Give the extent of all Plasmodium falciparum-infected red blood cells.
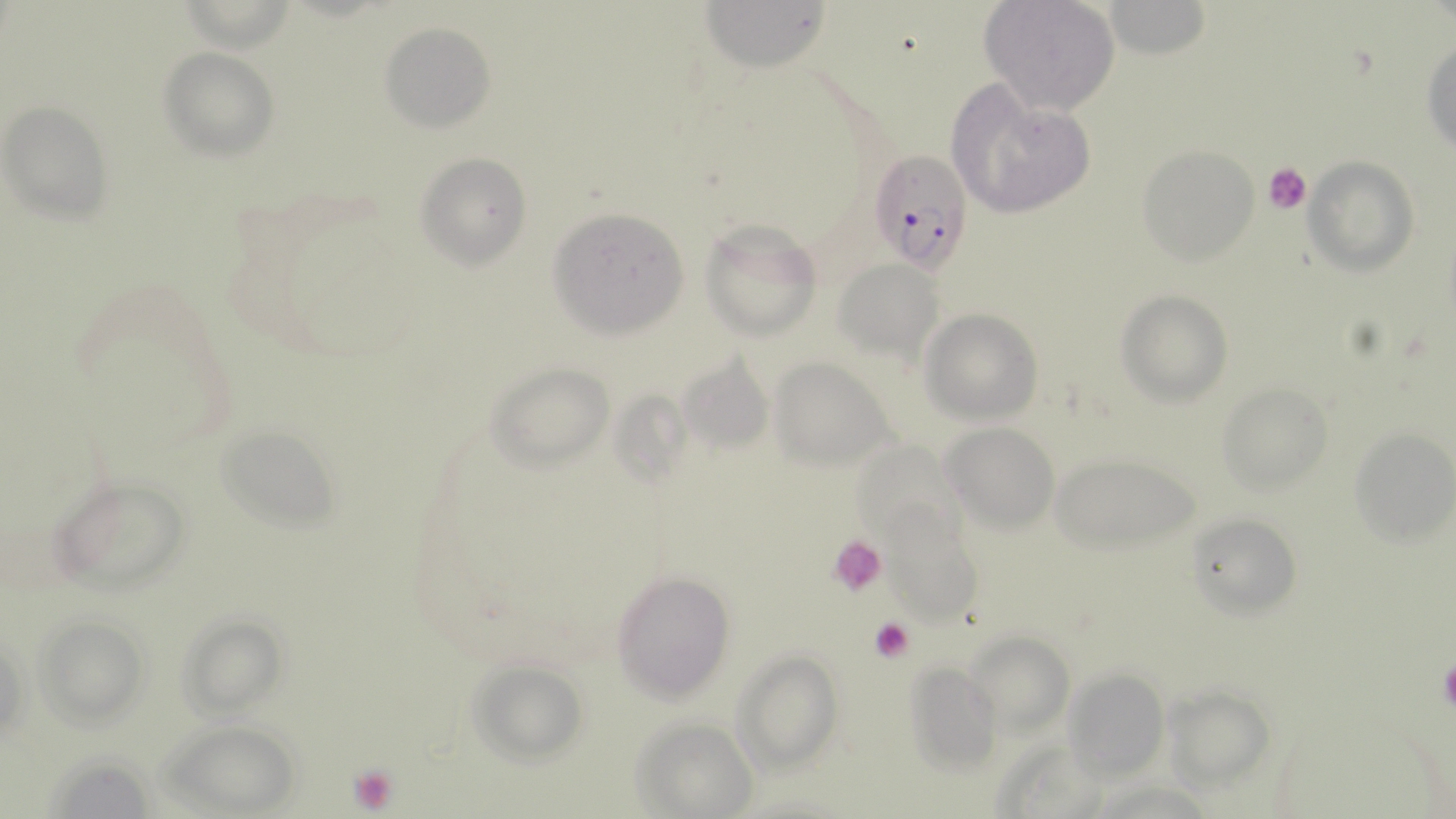

Approximate bounding boxes as (x1,y1)-(x2,y2) corner pairs in pixels.
Plasmodium falciparum-infected red blood cells: (869,148)-(974,273).

slide-level diagnosis = Plasmodium falciparum
magnification = 1000x
uninfected red blood cell locations = approximate bounding boxes as (x1,y1)-(x2,y2) corner pairs in pixels: (700,0)-(832,70), (979,0)-(1120,115), (1099,0)-(1211,60), (380,22)-(496,132), (1422,35)-(1455,157), (159,47)-(279,160), (946,83)-(1099,220), (2,102)-(113,223), (1137,144)-(1259,264), (416,151)-(532,269), (1306,157)-(1418,273), (548,206)-(689,337), (699,219)-(822,340), (835,258)-(946,358), (1118,290)-(1232,405), (920,308)-(1042,425), (677,349)-(774,460), (769,357)-(894,470), (487,361)-(615,469), (1218,382)-(1333,495), (942,423)-(1060,532), (218,426)-(340,529), (1349,427)-(1455,548), (850,437)-(963,548), (1050,454)-(1199,553), (48,476)-(189,595), (1187,512)-(1303,618), (886,523)-(981,626), (613,571)-(733,701), (173,610)-(292,720), (35,616)-(151,729), (964,632)-(1073,733), (733,649)-(843,770), (900,660)-(1001,773), (466,661)-(588,766), (1063,667)-(1169,781), (1162,685)-(1278,790), (630,714)-(762,818), (163,719)-(302,816)
field of view = single
modality = optical microscopy
image size = 1456×819 pixels
preparation = thin blood film
stain = May-Grünwald-Giemsa
platelet locations = approximate bounding boxes as (x1,y1)-(x2,y2) corner pairs in pixels: (1263,162)-(1312,213), (829,535)-(885,597), (870,617)-(915,664), (1437,656)-(1456,711), (347,762)-(399,813)